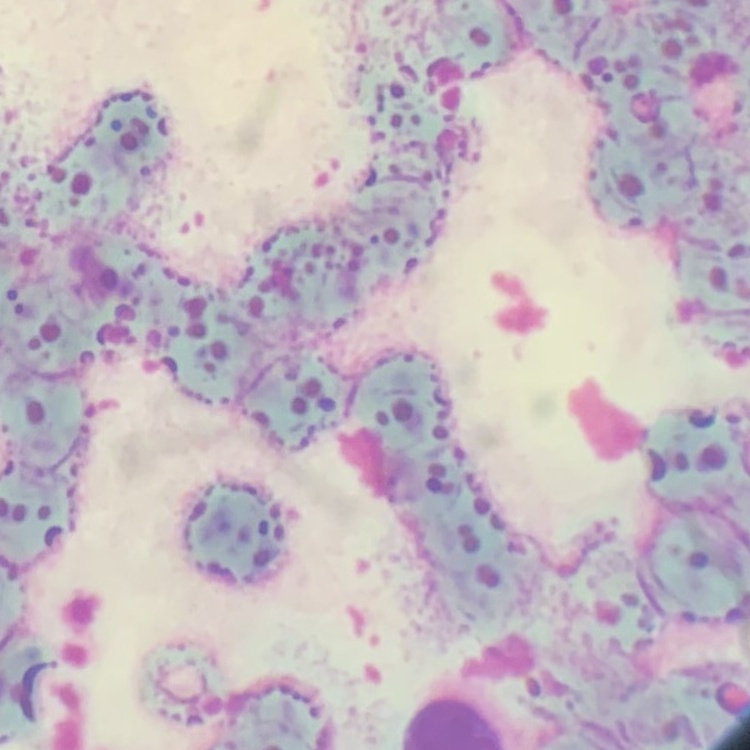
{
  "red_blood_cell_morphology": "rouleaux formation",
  "stain": "Field's or Giemsa",
  "preparation": "thin blood film",
  "image_type": "one tile cut from a larger photomicrograph"
}